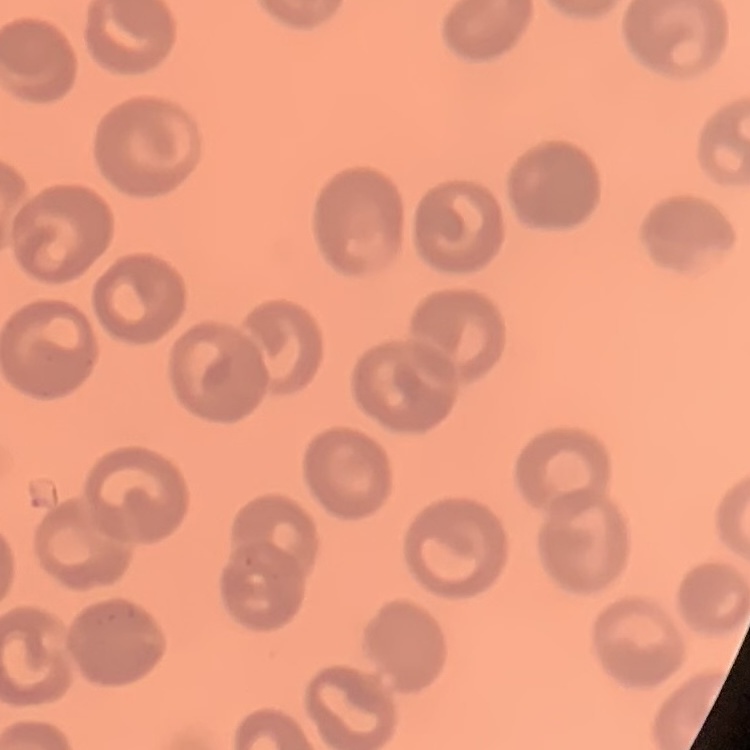
The red blood cells show no rouleaux formation. One tile cut from a larger photomicrograph. Thin blood film. Stained with either Field's or Giemsa.